Report the malaria status of this cell.
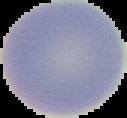

It is uninfected.

image type = segmented cell region with the area outside set to black
preparation = thin blood film
image size = 127×118 pixels